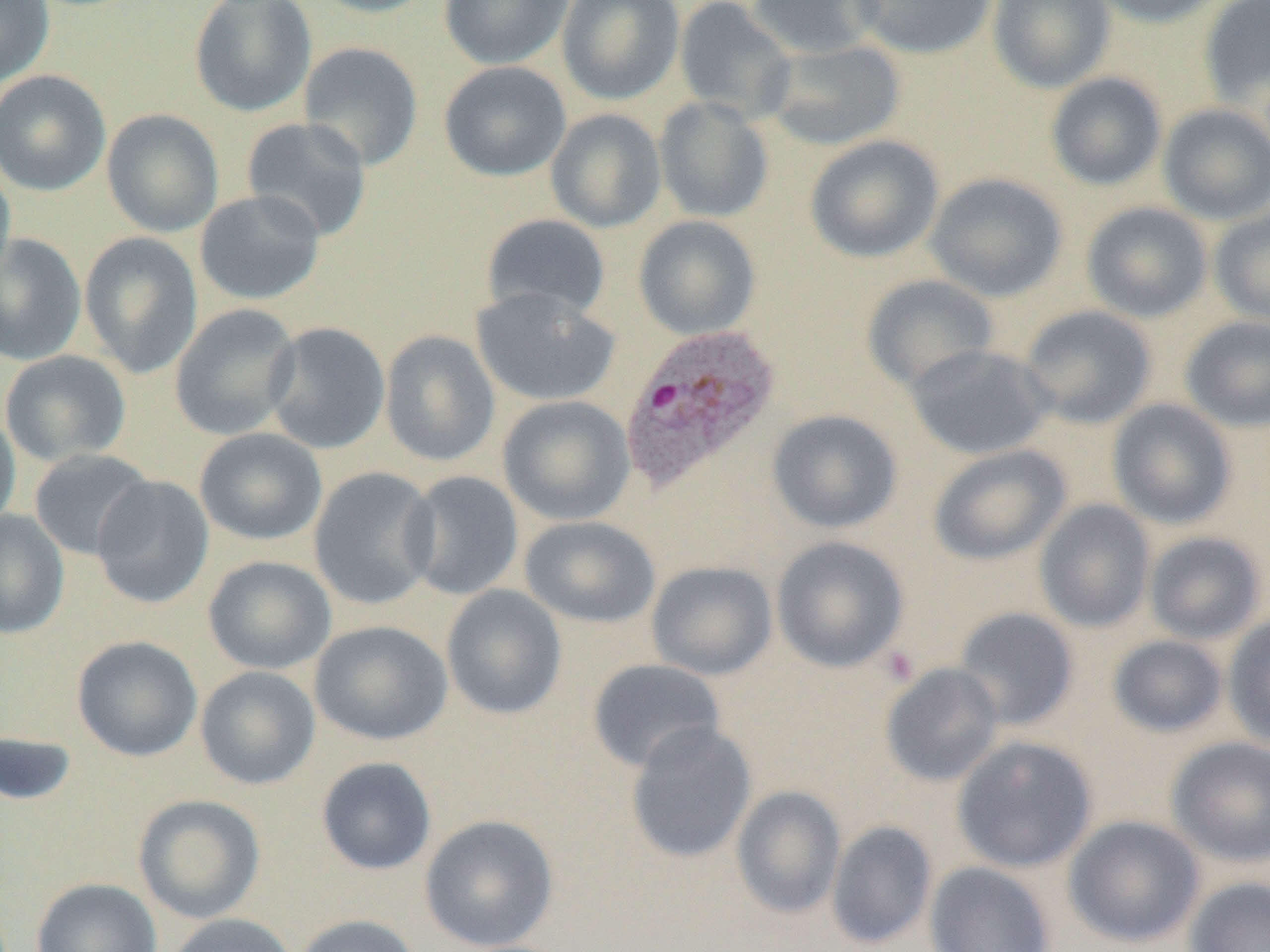 Approximate bounding boxes as (x1, y1, x2, y2) in pixels. Plasmodium ovale-infected red blood cell locations: (619, 324, 781, 495). Uninfected red blood cell locations: (0, 0, 54, 89), (309, 0, 443, 18), (439, 0, 573, 70), (557, 0, 685, 105), (674, 0, 797, 123), (745, 0, 887, 60), (850, 0, 997, 59), (987, 0, 1115, 93), (1089, 0, 1227, 27), (1199, 0, 1270, 106), (189, 1, 317, 117), (763, 39, 906, 151), (298, 41, 424, 171), (439, 61, 571, 181), (0, 69, 111, 196), (1046, 72, 1167, 191), (653, 96, 774, 223), (1157, 103, 1270, 225), (102, 108, 224, 238), (545, 108, 667, 233), (240, 116, 372, 241), (805, 135, 945, 263), (0, 157, 15, 289), (925, 172, 1068, 302), (194, 189, 325, 305), (1081, 201, 1213, 323), (1209, 209, 1270, 326), (481, 213, 611, 321), (633, 215, 761, 340), (79, 232, 203, 379), (0, 233, 86, 366), (860, 274, 999, 392), (470, 286, 619, 407), (169, 303, 302, 440), (1019, 305, 1156, 429), (1180, 316, 1270, 432), (263, 322, 391, 454), (379, 330, 500, 467), (905, 343, 1054, 460), (0, 350, 131, 467), (497, 395, 636, 526), (1107, 398, 1237, 529), (0, 406, 21, 534), (767, 409, 903, 534), (194, 427, 327, 545), (928, 445, 1072, 565), (29, 448, 155, 561), (309, 466, 440, 610), (402, 470, 524, 600), (90, 475, 214, 609), (1034, 499, 1155, 632), (0, 508, 69, 639), (519, 515, 660, 629), (1144, 530, 1267, 645), (771, 536, 909, 673), (202, 555, 336, 675), (646, 560, 778, 681), (441, 585, 567, 720), (953, 607, 1079, 731), (1223, 613, 1270, 749), (309, 620, 453, 745), (1108, 635, 1228, 738), (72, 636, 203, 762), (587, 658, 726, 774), (880, 663, 1004, 787), (195, 666, 320, 790), (625, 721, 757, 864), (0, 729, 78, 807), (952, 735, 1098, 873), (1167, 737, 1270, 867), (315, 757, 437, 876), (731, 785, 846, 919), (133, 794, 265, 925), (419, 814, 559, 950), (1063, 814, 1205, 948), (826, 821, 937, 949), (924, 861, 1056, 952), (31, 877, 162, 952), (1183, 877, 1270, 952), (160, 913, 300, 952), (291, 914, 422, 952). Platelet locations: (880, 645, 920, 687). Slide-level diagnosis: Plasmodium ovale. Image is 1270×952 pixels. 1000x magnification. Single field of view. Light microscopy. Thin blood smear.